Locate every Plasmodium falciparum-infected red blood cell.
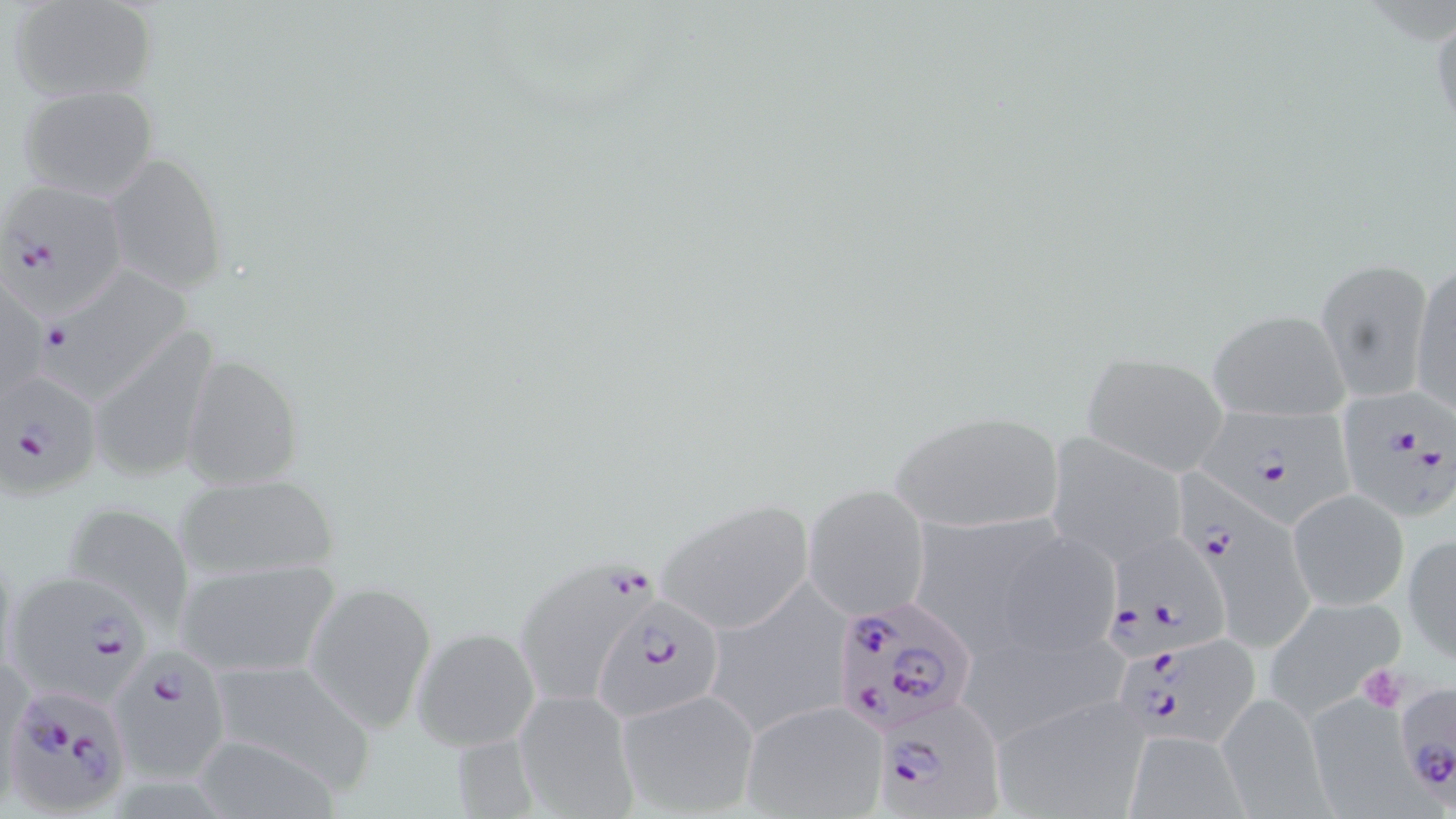

Approximate bounding boxes as (x1, y1, x2, y2) in pixels.
Plasmodium falciparum-infected red blood cells: (0, 181, 127, 317), (31, 268, 196, 410), (0, 371, 103, 498), (1329, 392, 1456, 520), (1193, 394, 1363, 538), (1172, 462, 1327, 658), (1109, 520, 1223, 658), (512, 556, 660, 710), (4, 568, 152, 703), (593, 595, 726, 723), (833, 595, 975, 739), (1118, 633, 1267, 745), (105, 645, 232, 784), (0, 686, 128, 819), (1409, 690, 1456, 810), (871, 694, 1003, 815).

slide-level diagnosis = Plasmodium falciparum
field of view = single
modality = optical microscopy
magnification = 1000x
image size = 1456×819 pixels
preparation = thin blood smear
uninfected red blood cell locations = approximate bounding boxes as (x1, y1, x2, y2) in pixels: (8, 1, 159, 102), (1429, 11, 1456, 146), (15, 83, 160, 200), (103, 152, 228, 294), (1409, 256, 1455, 417), (1315, 257, 1433, 402), (1, 272, 46, 410), (1208, 308, 1352, 421), (88, 324, 220, 485), (1080, 351, 1231, 476), (179, 354, 303, 492), (886, 408, 1067, 535), (1046, 434, 1187, 568), (171, 472, 342, 581), (803, 484, 930, 621), (1289, 486, 1408, 611), (658, 498, 815, 633), (59, 500, 198, 627), (912, 500, 1064, 643), (991, 529, 1120, 657), (1404, 533, 1456, 661), (174, 555, 343, 681), (720, 576, 865, 731), (304, 579, 438, 734), (1264, 595, 1407, 717), (412, 626, 540, 752), (961, 629, 1131, 744), (204, 654, 375, 793), (511, 687, 638, 819), (615, 689, 761, 818), (1308, 690, 1437, 818), (1216, 691, 1330, 815), (990, 696, 1150, 818), (740, 700, 887, 819), (1123, 732, 1244, 816)
stain = May-Grünwald-Giemsa
platelet locations = approximate bounding boxes as (x1, y1, x2, y2) in pixels: (1354, 663, 1410, 713)